Name the parasite shown.
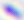

This is Toxoplasma gondii.

magnification = 400x
modality = micrograph